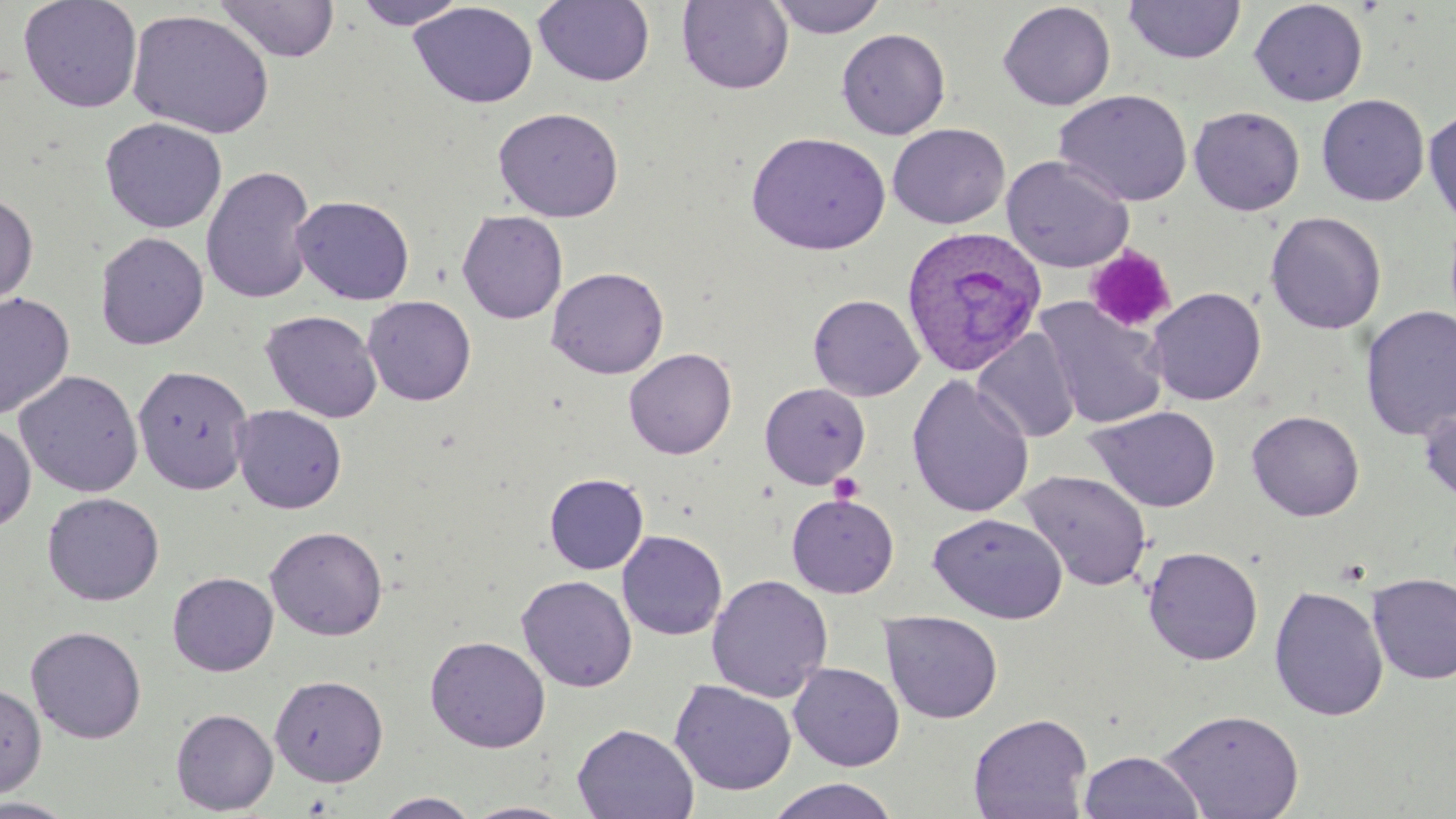

Summary:
  - Coordinate format: approximate bounding boxes as (x1,y1)-(x2,y2) corner pairs in pixels
  - Plasmodium ovale-infected red blood cell locations: (899,225)-(1047,377)
  - Platelet locations: (1084,245)-(1177,334), (828,472)-(865,504)
  - Uninfected red blood cell locations: (17,0)-(143,113), (352,0)-(470,30), (766,0)-(889,38), (1123,0)-(1246,64), (213,1)-(340,62), (533,1)-(655,87), (676,1)-(794,94), (997,1)-(1116,111), (1249,1)-(1368,107), (408,2)-(538,109), (127,9)-(275,139), (836,27)-(951,140), (1054,89)-(1193,207), (1316,93)-(1430,207), (1189,106)-(1305,216), (493,107)-(624,222), (1424,107)-(1456,228), (99,117)-(228,234), (887,123)-(1010,229), (745,131)-(891,256), (1001,155)-(1134,272), (201,164)-(317,304), (0,192)-(38,310), (291,195)-(415,305), (456,209)-(569,324), (1264,211)-(1386,334), (94,231)-(209,350), (546,266)-(669,379), (1146,287)-(1267,406), (0,292)-(75,420), (808,294)-(924,400), (362,295)-(476,406), (1034,297)-(1168,429), (1360,305)-(1456,441), (260,310)-(383,423), (973,328)-(1081,443), (624,348)-(736,459), (132,365)-(254,494), (13,369)-(144,498), (907,374)-(1034,518), (759,382)-(871,489), (1419,401)-(1456,507), (231,404)-(347,514), (1086,405)-(1221,513), (1246,410)-(1365,521), (0,422)-(36,532), (1019,470)-(1153,592), (544,473)-(649,575), (42,492)-(165,606), (786,494)-(899,598), (928,512)-(1068,623), (265,526)-(388,640), (617,530)-(727,641), (1142,546)-(1264,666), (167,571)-(279,676), (1367,572)-(1456,684), (706,574)-(833,702), (516,575)-(637,692), (1269,585)-(1388,722), (880,611)-(1003,724), (26,626)-(147,744), (425,635)-(551,753), (788,662)-(905,771), (269,674)-(388,786), (669,680)-(797,796), (0,682)-(47,800), (171,708)-(278,814), (1157,708)-(1304,819), (968,713)-(1092,819), (571,723)-(699,819), (1078,749)-(1204,819), (766,778)-(900,819), (373,792)-(483,818), (0,798)-(81,818), (461,801)-(577,818)
  - Slide-level diagnosis: Plasmodium ovale
  - Modality: light microscopy
  - Preparation: thin blood film
  - Image size: 1456×819 pixels
  - Stain: May-Grünwald-Giemsa
  - Magnification: 1000x
  - Field of view: one of a larger specimen